Identify the preparation type.
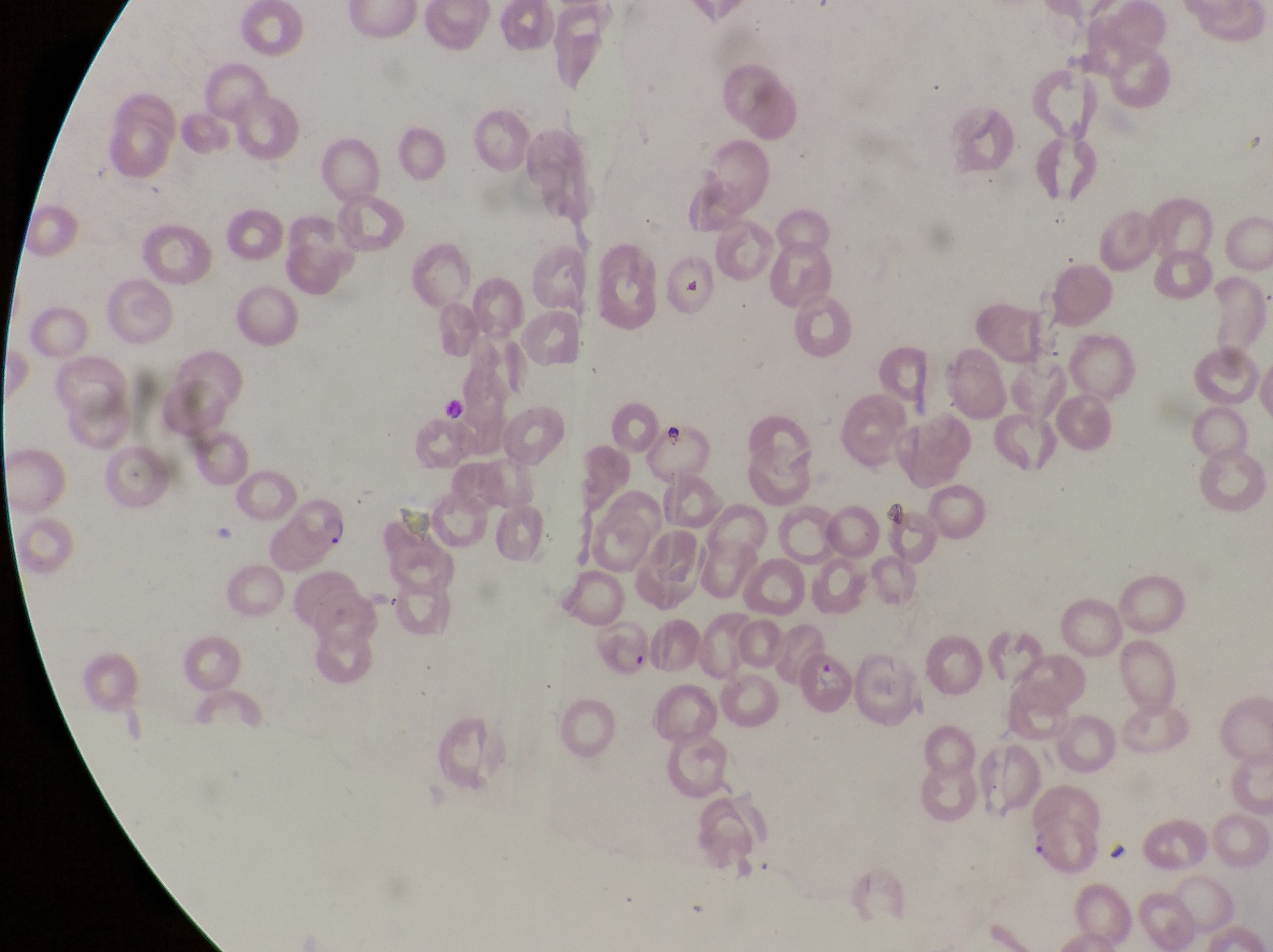
Thin blood smear.

Approximate bounding boxes as {left, top, right, bottom} in pixels.
Summary:
  - Parasitised red blood cell locations: {287, 495, 357, 562}, {803, 646, 860, 720}, {1018, 822, 1101, 880}
  - Artifact (platelet-like body, stain precipitate, or debris) locations: {661, 419, 691, 451}, {882, 500, 915, 531}
  - Capture: smartphone photograph through the eyepiece of an Olympus CX-23 microscope
  - Country: Uganda
  - Image size: 1273×952 pixels
  - Field of view: single
  - Magnification: 1000x